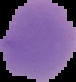
{
  "image_size": "76×82 pixels",
  "result": "negative for Plasmodium parasites",
  "preparation": "thin blood smear",
  "image_type": "segmented cell region with the area outside set to black"
}